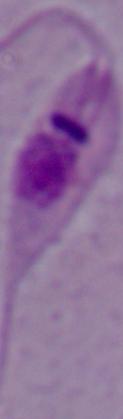

A Leishmania parasite is shown. 1000x magnification. Photomicrograph.